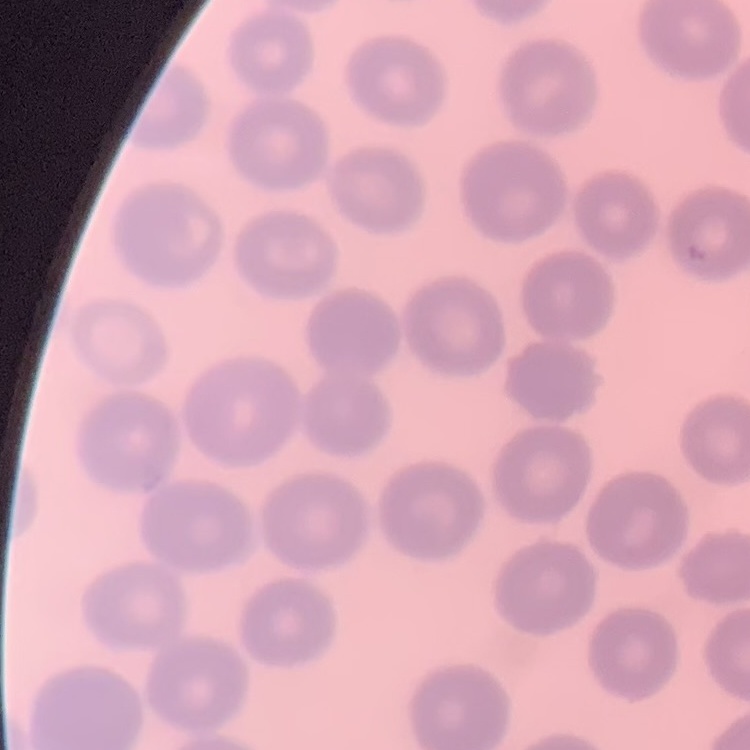 The erythrocytes show no rouleaux formation. One tile cut from a larger photomicrograph. Stained with either Field's or Giemsa. Thin blood film.